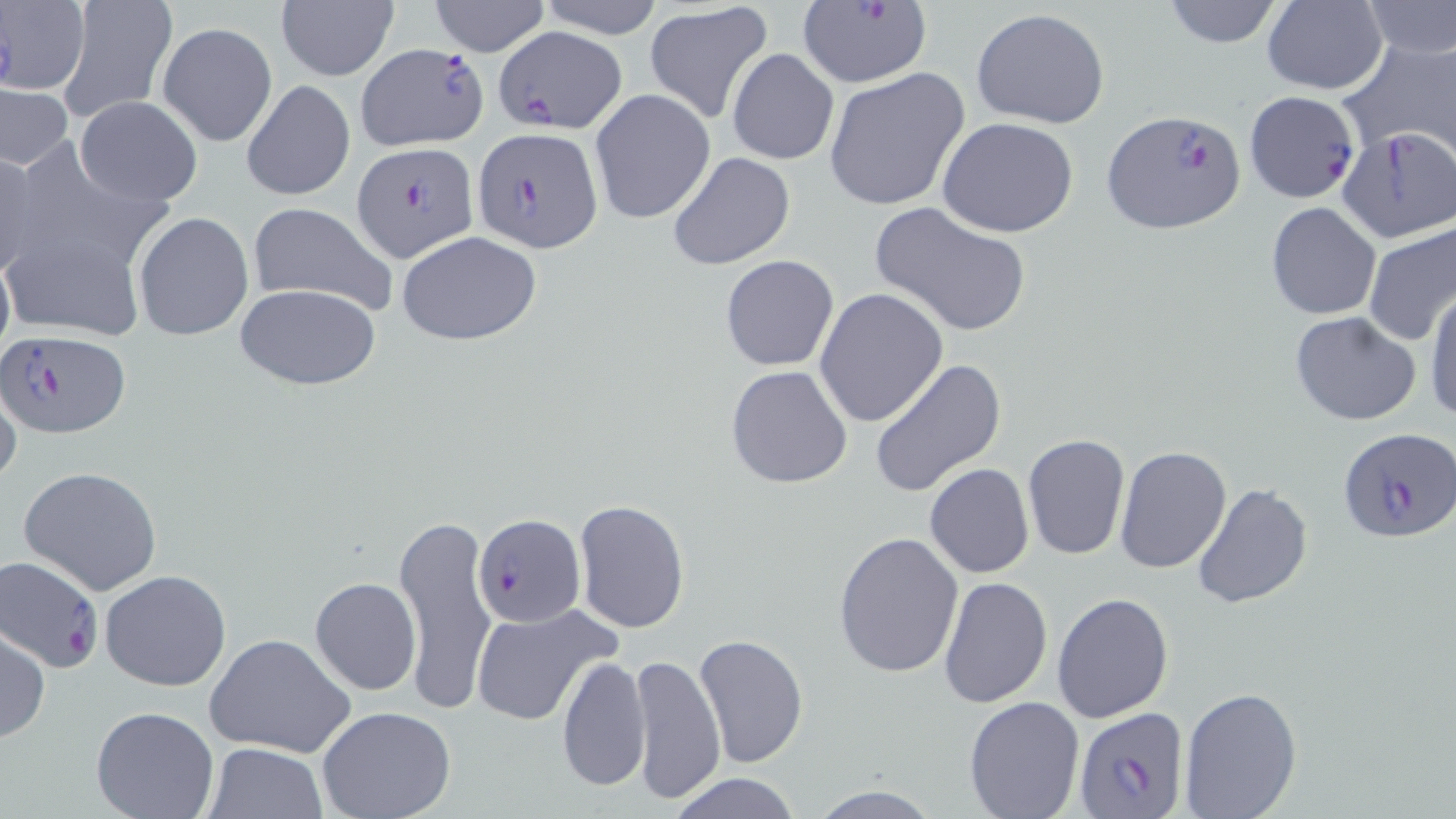 Approximate bounding boxes as [x1, y1, x2, y2] in pixels. Plasmodium falciparum-infected red blood cell locations (subset): [794, 0, 932, 87], [496, 27, 625, 134], [355, 42, 489, 151], [1100, 108, 1245, 235], [471, 126, 603, 251], [352, 143, 479, 263], [0, 329, 131, 438], [1338, 428, 1456, 544], [475, 513, 583, 628], [1, 554, 104, 674], [1074, 706, 1189, 819]. Uninfected red blood cell locations (subset): [0, 0, 89, 96], [56, 0, 177, 124], [429, 0, 551, 56], [535, 0, 668, 39], [1158, 0, 1286, 49], [1263, 0, 1388, 96], [1358, 1, 1456, 59], [276, 2, 399, 82], [644, 3, 775, 124], [971, 9, 1112, 130], [159, 22, 277, 146], [1339, 35, 1456, 166], [727, 47, 839, 165], [823, 67, 969, 212], [241, 79, 355, 202], [0, 83, 74, 170], [589, 89, 716, 226], [74, 95, 204, 206], [937, 117, 1079, 238], [1337, 127, 1455, 242], [0, 148, 38, 282], [666, 151, 796, 271], [869, 201, 1031, 337], [247, 202, 397, 317], [1266, 202, 1381, 320], [132, 212, 253, 341], [1362, 221, 1456, 350], [1, 229, 150, 341], [397, 231, 544, 345], [0, 246, 14, 374], [719, 255, 839, 372], [234, 282, 381, 389], [1425, 282, 1456, 424], [815, 289, 949, 429], [1288, 312, 1423, 425], [870, 359, 1006, 497], [725, 365, 854, 487], [0, 378, 22, 492], [1022, 433, 1131, 561], [1114, 446, 1231, 573], [18, 464, 164, 596], [924, 464, 1035, 579], [1191, 482, 1312, 610], [573, 499, 690, 633], [395, 515, 497, 714], [833, 531, 965, 678], [100, 569, 232, 691], [310, 576, 420, 694], [937, 576, 1053, 706], [1052, 592, 1175, 724], [469, 603, 619, 725], [0, 626, 50, 742], [204, 633, 357, 758], [695, 634, 808, 768], [629, 651, 726, 808], [556, 655, 651, 792], [1176, 685, 1304, 818], [963, 695, 1084, 818], [91, 707, 219, 819], [317, 708, 457, 819], [205, 742, 327, 819], [669, 773, 803, 819], [807, 784, 944, 819]. Slide-level diagnosis: Plasmodium falciparum. Image is 1456×819 pixels. Thin blood film. Light microscopy. May-Grünwald-Giemsa-stained preparation. Captured at 1000x magnification. One field of a larger specimen.